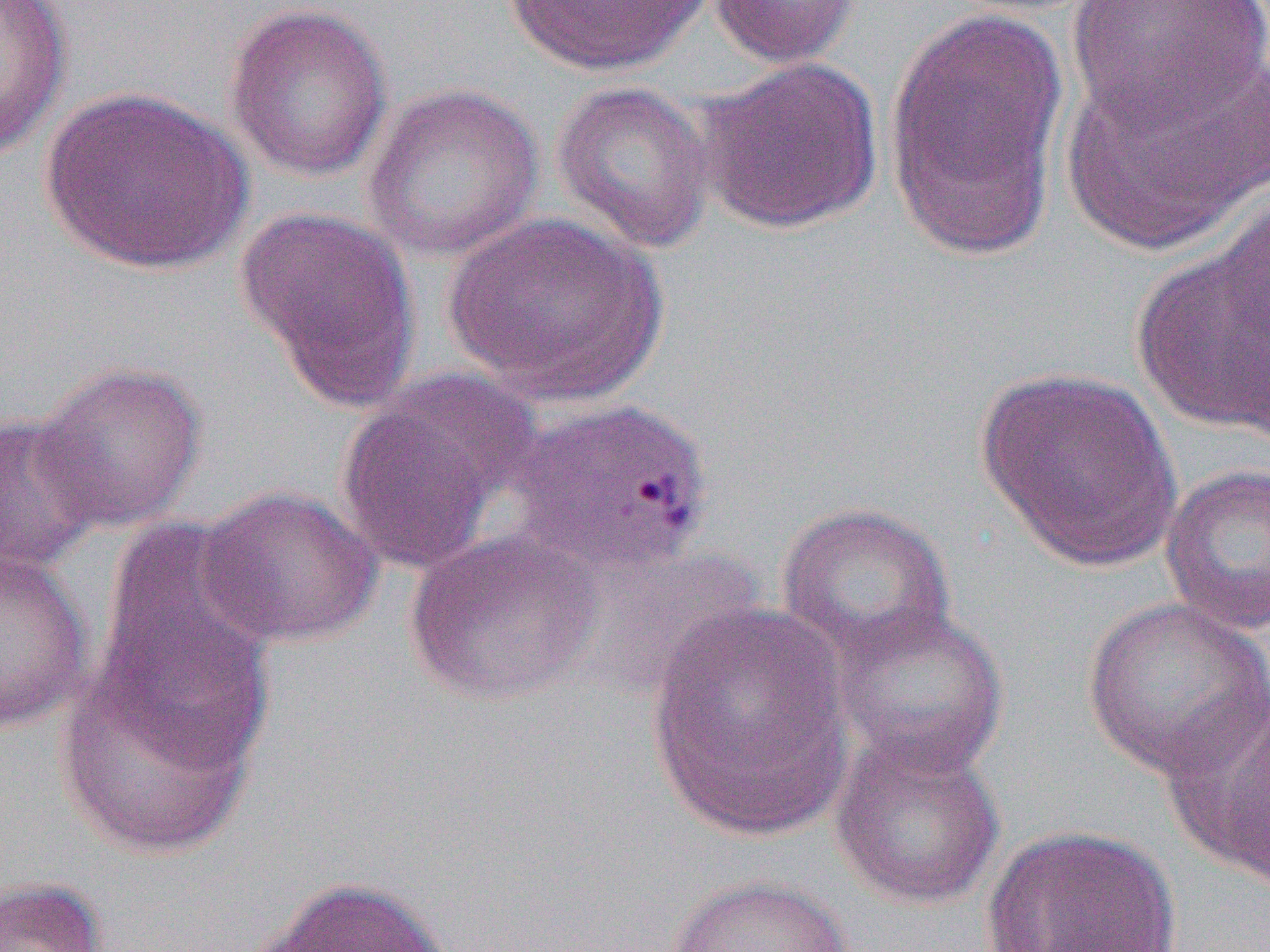

Approximate bounding boxes as [x1, y1, x2, y2] in pixels. Uninfected red blood cell locations: [0, 0, 72, 159], [501, 0, 714, 75], [707, 0, 863, 68], [1066, 0, 1269, 132], [223, 2, 393, 182], [883, 6, 1072, 261], [1061, 42, 1270, 256], [697, 56, 884, 235], [550, 80, 718, 254], [361, 82, 545, 263], [37, 86, 255, 275], [236, 206, 421, 408], [445, 212, 666, 406], [1131, 217, 1270, 438], [31, 361, 207, 532], [973, 367, 1182, 571], [335, 380, 525, 576], [0, 409, 104, 578], [1159, 462, 1270, 636], [197, 484, 383, 649], [776, 502, 957, 662], [89, 527, 278, 775], [404, 527, 603, 705], [0, 546, 93, 734], [1081, 596, 1270, 781], [647, 601, 857, 840], [828, 601, 1011, 776], [55, 665, 258, 857], [1160, 687, 1270, 881], [828, 727, 1005, 910], [980, 825, 1184, 951], [665, 874, 856, 952], [257, 875, 453, 951], [0, 876, 109, 952]. Slide-level diagnosis: Plasmodium vivax. Light microscopy. Single field of view. Captured at 1000x magnification. Thin blood film. Image is 1270×952 pixels.